Locate every Plasmodium ovale-infected red blood cell.
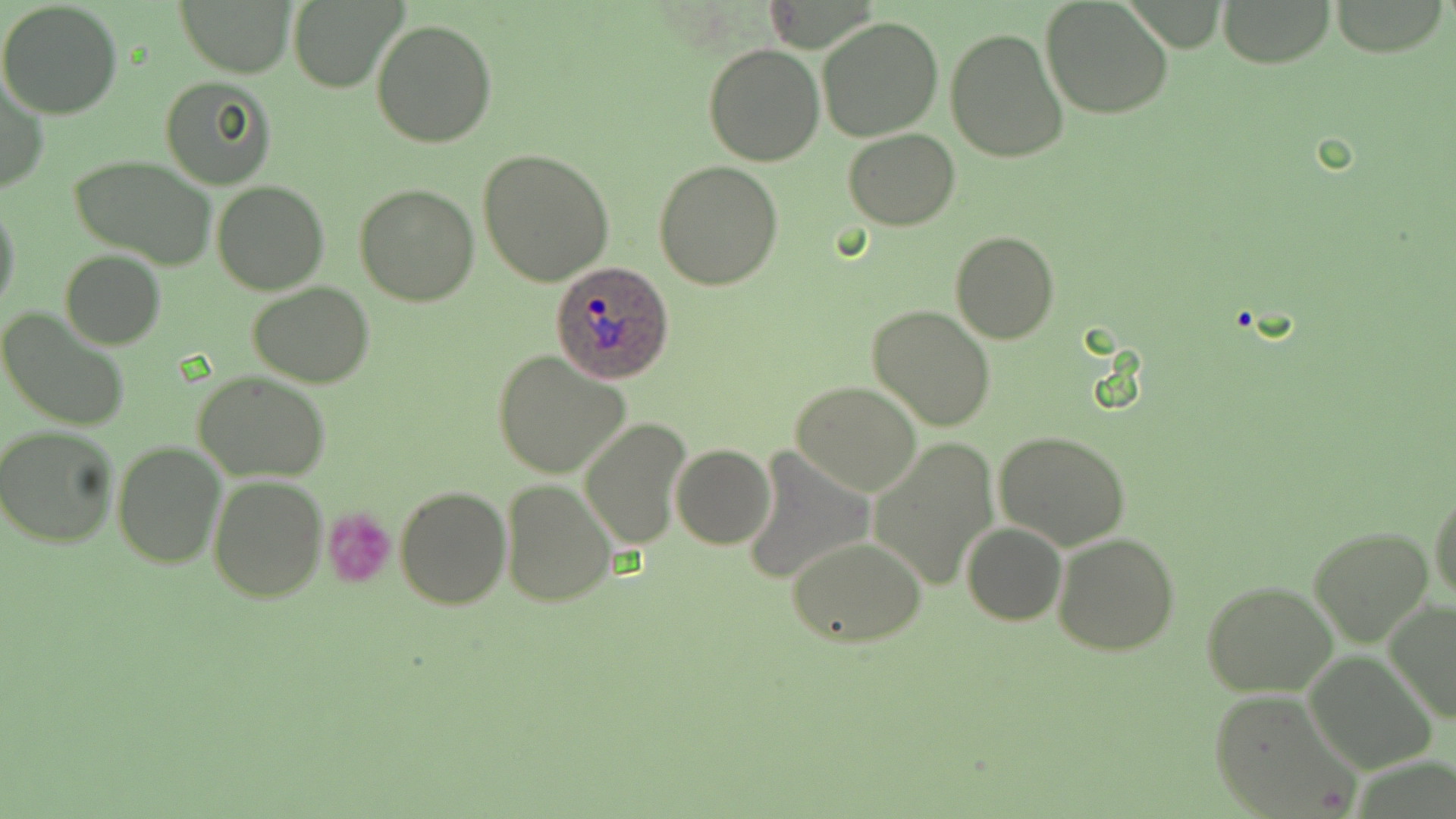

Approximate bounding boxes as [x1, y1, x2, y2] in pixels.
Plasmodium ovale-infected red blood cells: [551, 259, 675, 383].

slide-level diagnosis = Plasmodium ovale
modality = light microscopy
stain = May-Grünwald-Giemsa
image size = 1456×819 pixels
field of view = single
preparation = thin blood smear
uninfected red blood cell locations = approximate bounding boxes as [x1, y1, x2, y2] in pixels: [176, 0, 299, 76], [1041, 0, 1174, 121], [1217, 0, 1337, 67], [0, 1, 123, 118], [288, 1, 401, 91], [818, 15, 944, 141], [369, 19, 497, 149], [945, 28, 1069, 163], [703, 43, 825, 166], [159, 76, 277, 189], [0, 78, 48, 196], [843, 129, 961, 230], [479, 149, 615, 286], [71, 154, 216, 269], [653, 160, 783, 291], [212, 180, 328, 295], [354, 182, 479, 307], [0, 198, 21, 317], [950, 231, 1059, 344], [61, 250, 165, 348], [247, 281, 375, 387], [867, 304, 996, 431], [0, 306, 130, 433], [491, 351, 630, 480], [195, 371, 330, 480], [792, 382, 921, 496], [581, 419, 689, 549], [0, 426, 120, 548], [994, 431, 1133, 551], [869, 436, 1000, 592], [111, 442, 226, 570], [672, 443, 775, 550], [741, 448, 874, 587], [207, 475, 327, 603], [500, 478, 615, 607], [394, 485, 511, 609], [1430, 488, 1456, 606], [962, 522, 1066, 626], [1309, 526, 1434, 648], [1053, 531, 1181, 657], [785, 536, 928, 648], [1201, 580, 1338, 698], [1383, 598, 1456, 724], [1304, 651, 1437, 773], [1208, 689, 1358, 817]
magnification = 1000x
platelet locations = approximate bounding boxes as [x1, y1, x2, y2] in pixels: [322, 508, 397, 589]